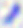

Summary:
  - Modality: micrograph
  - Magnification: 400x
  - Identification: Toxoplasma gondii